Report the malaria status of this cell.
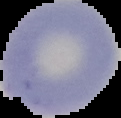

Uninfected.

Summary:
  - Image type: segmented cell region with the area outside set to black
  - Image size: 121×118 pixels
  - Preparation: thin blood film